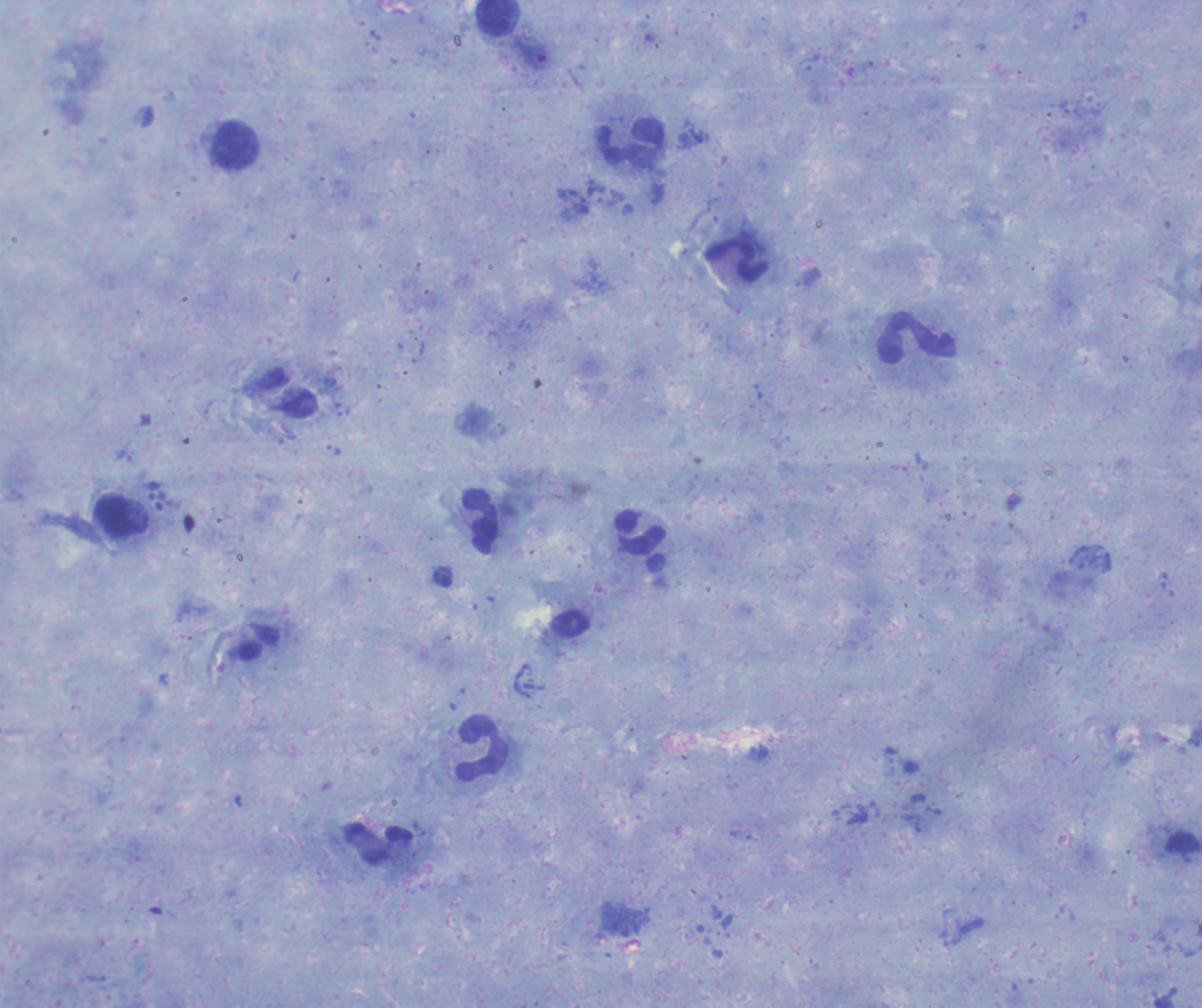

Approximate object centers, in pixels from the top-left corner.
Summary:
  - Leukocyte locations: (x=497, y=18), (x=632, y=143), (x=234, y=147), (x=737, y=260), (x=918, y=339), (x=119, y=517), (x=480, y=523), (x=641, y=542), (x=483, y=748)
  - Result: no malaria parasites detected
  - Magnification: 100x
  - Preparation: thick blood film
  - Field of view: one from this slide
  - Image size: 1202×1008 pixels
  - Stain: Romanowsky
  - Background quality: good
  - Context: previously used in an actual diagnosis
  - Coloration quality: good